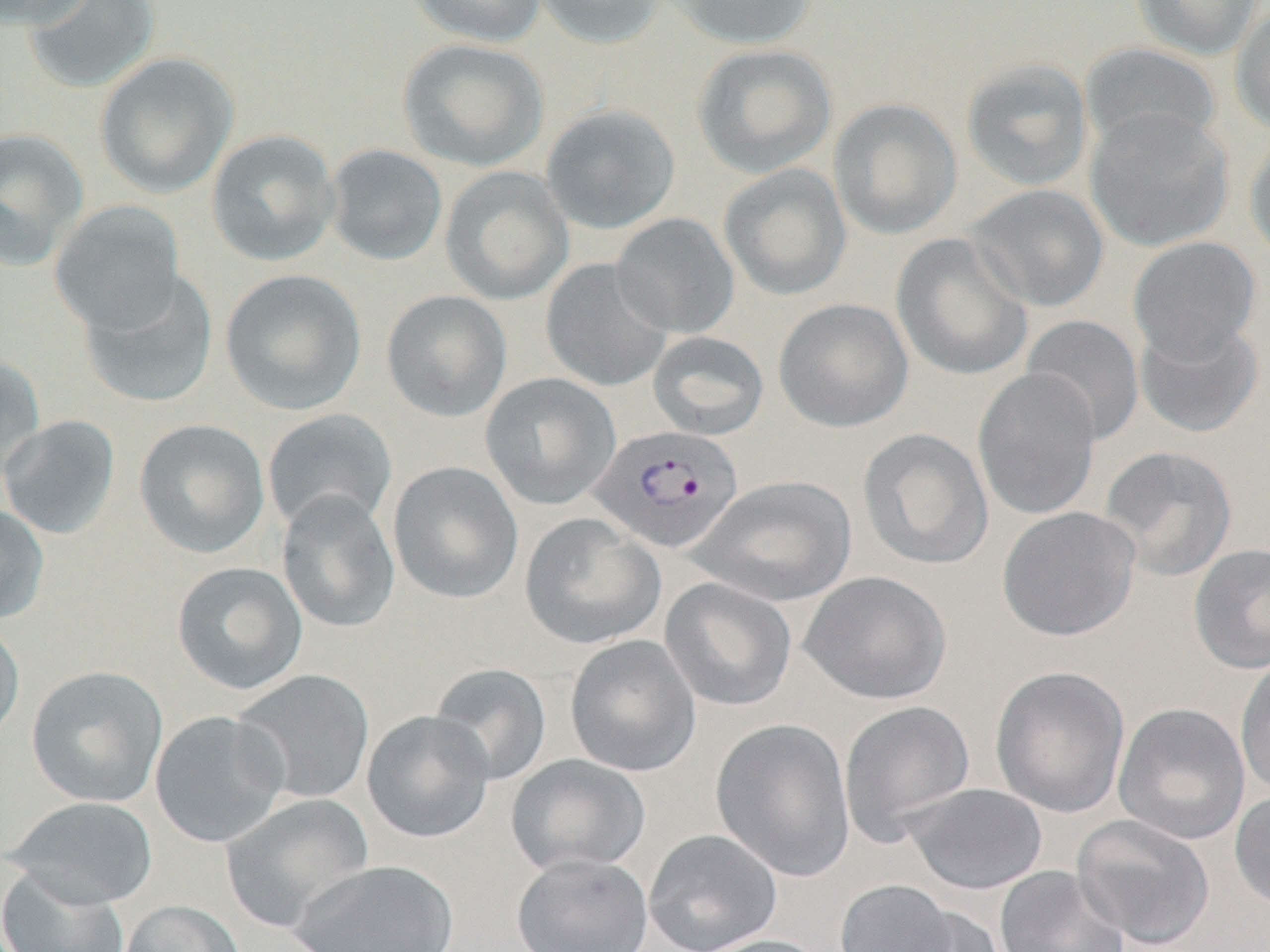 Approximate bounding boxes as [x1, y1, x2, y2] in pixels. Uninfected red blood cell locations: [0, 0, 97, 30], [22, 0, 160, 94], [407, 0, 546, 47], [533, 0, 668, 49], [667, 0, 818, 49], [1132, 0, 1263, 60], [1229, 4, 1270, 134], [397, 38, 549, 172], [1079, 42, 1222, 156], [692, 43, 837, 177], [95, 52, 239, 198], [960, 57, 1094, 192], [829, 98, 962, 240], [540, 104, 680, 234], [1085, 107, 1234, 252], [1245, 127, 1270, 267], [0, 129, 88, 270], [207, 129, 340, 266], [324, 144, 448, 266], [719, 164, 852, 301], [440, 166, 574, 305], [966, 184, 1109, 313], [50, 200, 185, 334], [611, 213, 739, 338], [891, 233, 1034, 382], [1128, 236, 1262, 364], [540, 258, 673, 393], [220, 269, 367, 416], [78, 270, 218, 409], [381, 290, 512, 422], [773, 298, 914, 432], [1021, 315, 1145, 446], [1135, 318, 1264, 438], [647, 330, 769, 441], [0, 354, 46, 486], [972, 368, 1102, 521], [480, 372, 621, 510], [262, 408, 397, 535], [0, 415, 120, 539], [133, 419, 270, 558], [857, 428, 994, 571], [1099, 445, 1239, 582], [388, 461, 523, 604], [692, 474, 857, 607], [276, 490, 400, 634], [0, 502, 49, 624], [997, 506, 1140, 642], [520, 513, 665, 650], [1188, 543, 1270, 674], [171, 561, 308, 695], [799, 571, 953, 705], [660, 577, 797, 712], [0, 616, 25, 749], [565, 634, 701, 777], [1234, 655, 1270, 798], [428, 663, 553, 786], [26, 665, 168, 807], [990, 665, 1130, 818], [232, 669, 375, 804], [838, 699, 976, 846], [1113, 702, 1251, 845], [362, 709, 495, 843], [149, 710, 289, 849], [710, 717, 856, 881], [505, 753, 650, 875], [903, 783, 1047, 895], [1230, 788, 1270, 911], [220, 793, 374, 933], [5, 796, 160, 909], [1072, 814, 1215, 950], [643, 829, 782, 952], [512, 853, 653, 951], [290, 860, 460, 952], [994, 865, 1129, 952], [0, 866, 129, 952], [835, 879, 960, 952], [118, 900, 245, 952], [897, 905, 1005, 952], [697, 934, 833, 952]. Plasmodium vivax-infected red blood cell locations: [591, 424, 743, 555]. Slide-level diagnosis: Plasmodium vivax. One field of a larger specimen. Thin blood film. Image is 1270×952 pixels. May-Grünwald-Giemsa-stained preparation. Optical microscopy. 1000x magnification.